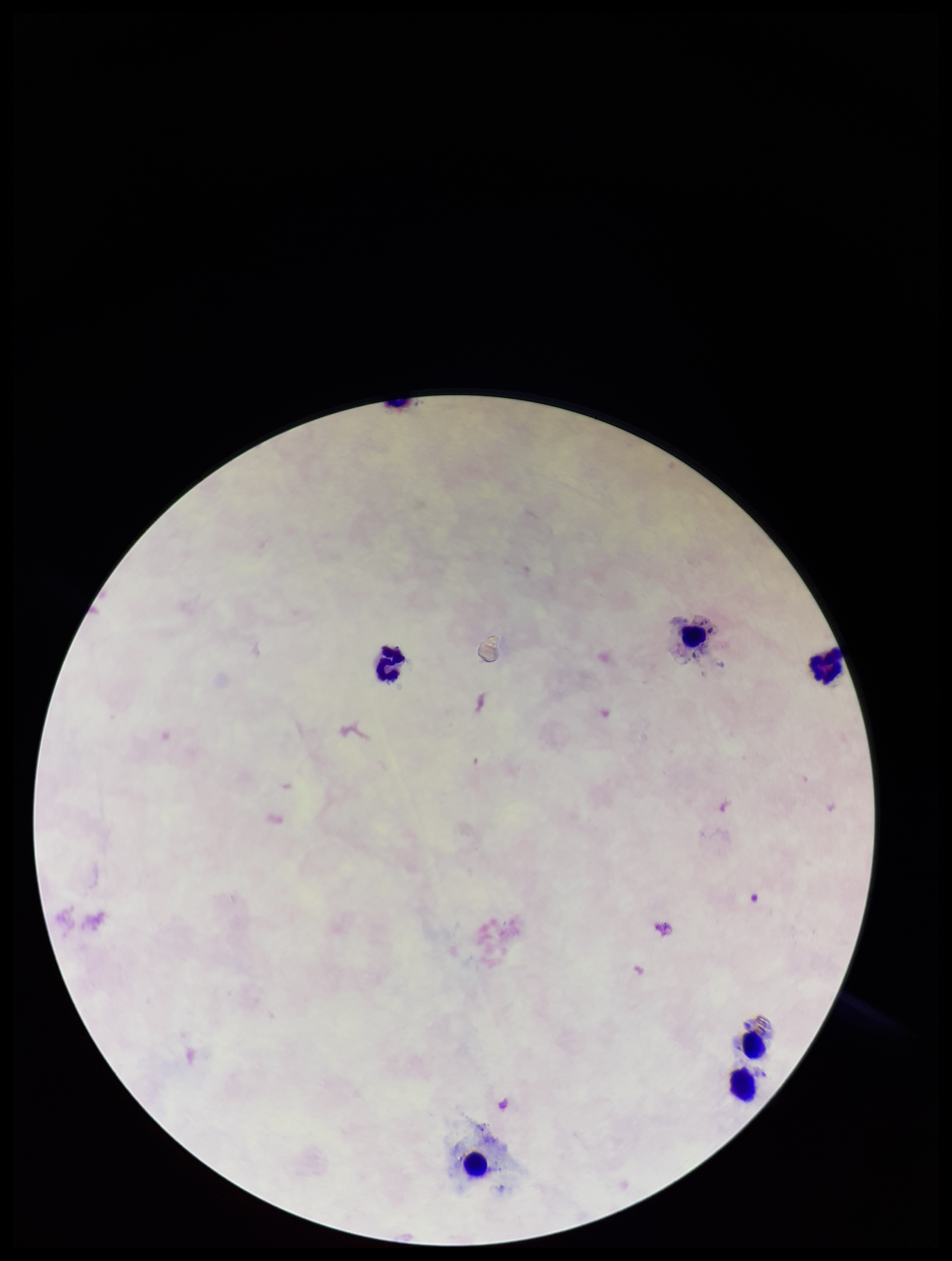

Summary:
  - Image size: 952×1261 pixels
  - Stain: Giemsa
  - Plasmodium parasites: none seen
  - Field of view: single
  - Preparation: thick
  - Leukocyte count: 6
  - Capture: smartphone photograph through the microscope eyepiece
  - Patient malaria status: negative
  - Parasite count: 0